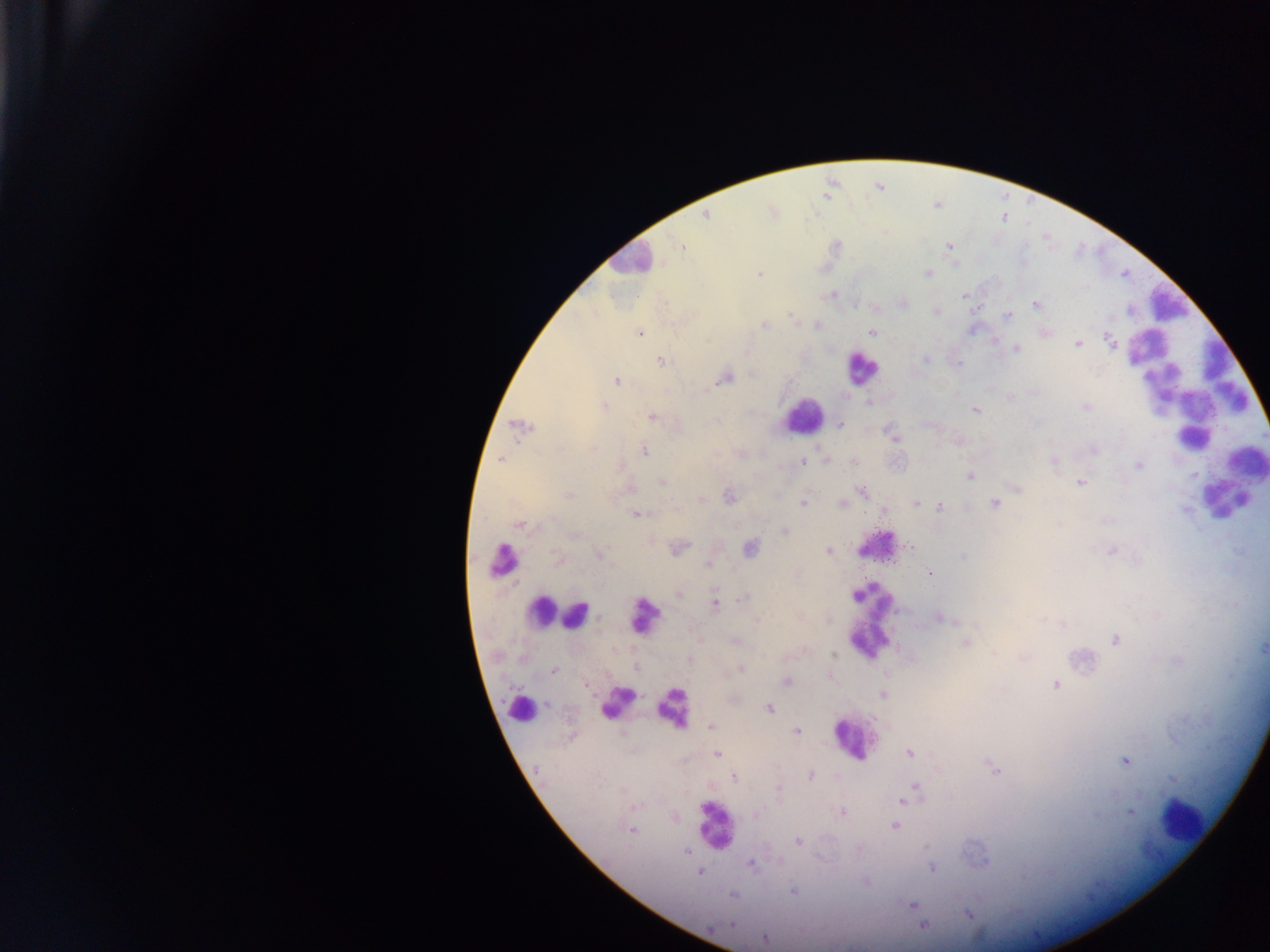
{
  "capture": "mobile-phone photograph through a microscope",
  "leukocyte_locations": "approximate centers as {x, y} in pixels: {630, 258}, {1169, 305}, {861, 369}, {1192, 386}, {802, 416}, {1222, 501}, {875, 546}, {500, 559}, {540, 610}, {576, 615}, {642, 617}, {870, 622}, {618, 700}, {519, 702}, {672, 709}, {853, 740}, {1182, 817}, {714, 825}",
  "country": "Ghana",
  "field_of_view": "single",
  "preparation": "thick blood film",
  "image_size": "1270×952 pixels",
  "malaria_parasite_locations": "approximate centers as {x, y} in pixels: {705, 215}, {682, 246}, {950, 247}, {928, 273}, {760, 274}, {832, 295}, {963, 295}, {904, 304}, {1035, 304}, {937, 311}, {1008, 316}, {794, 318}, {764, 325}, {817, 326}, {639, 332}, {871, 332}, {1110, 341}, {1078, 344}, {1016, 348}, {926, 358}, {661, 361}, {725, 378}, {617, 380}, {869, 404}, {1085, 406}, {604, 407}, {975, 411}, {651, 417}, {840, 425}, {520, 426}, {891, 434}, {1093, 450}, {644, 451}, {501, 459}, {1053, 460}, {803, 462}, {853, 462}, {1139, 466}, {970, 476}, {663, 482}, {1081, 483}, {1017, 489}, {862, 492}, {568, 495}, {730, 497}, {701, 499}, {803, 502}, {916, 503}, {843, 504}, {995, 504}, {941, 507}, {676, 509}, {884, 511}, {635, 514}, {519, 525}, {785, 531}, {575, 535}, {910, 547}, {679, 548}, {750, 548}, {828, 551}, {1111, 551}, {600, 554}, {964, 556}, {557, 559}, {708, 565}, {929, 573}, {679, 593}, {745, 597}, {715, 604}, {941, 618}, {757, 621}, {1114, 640}, {735, 641}, {965, 643}, {1263, 648}, {995, 653}, {833, 655}, {690, 659}, {636, 668}, {740, 669}, {554, 670}, {786, 682}, {1055, 685}, {883, 695}, {769, 708}, {711, 727}, {796, 730}, {717, 754}, {909, 754}, {1125, 761}, {994, 769}, {811, 775}, {734, 777}, {1172, 779}, {915, 786}, {779, 788}, {902, 801}, {635, 807}, {842, 812}, {1131, 812}, {757, 815}, {894, 826}, {632, 830}, {798, 842}, {685, 852}, {750, 864}, {932, 867}, {699, 873}, {867, 883}, {793, 891}, {732, 896}, {912, 905}, {967, 914}, {732, 925}, {923, 926}, {765, 939}"
}